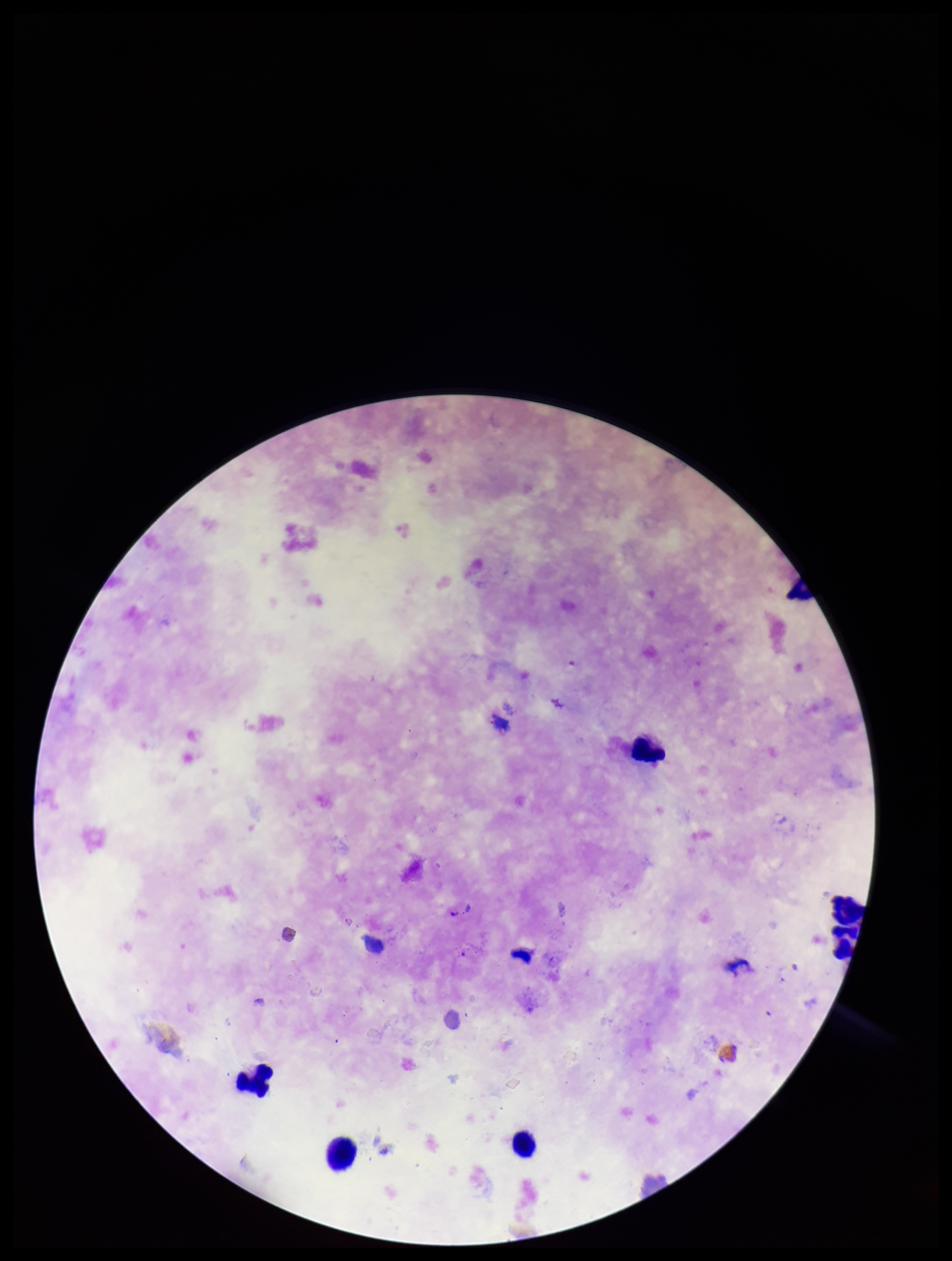 Giemsa stain. Preparation: thick smear. Plasmodium parasites: none seen. Image is 952×1261 pixels. Leukocyte count: 6. One field from this slide. Parasite count: 0. Smartphone photograph taken through the eyepiece of a microscope. Species reported for this patient: Plasmodium falciparum. Patient malaria status: infected.